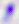 400x magnification. Toxoplasma gondii is seen. Micrograph.